State which cell type is depicted.
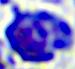
This is a leukocyte.

magnification = 400x
modality = micrograph